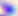
Summary:
  - Magnification: 400x
  - Modality: micrograph
  - Identification: Toxoplasma gondii